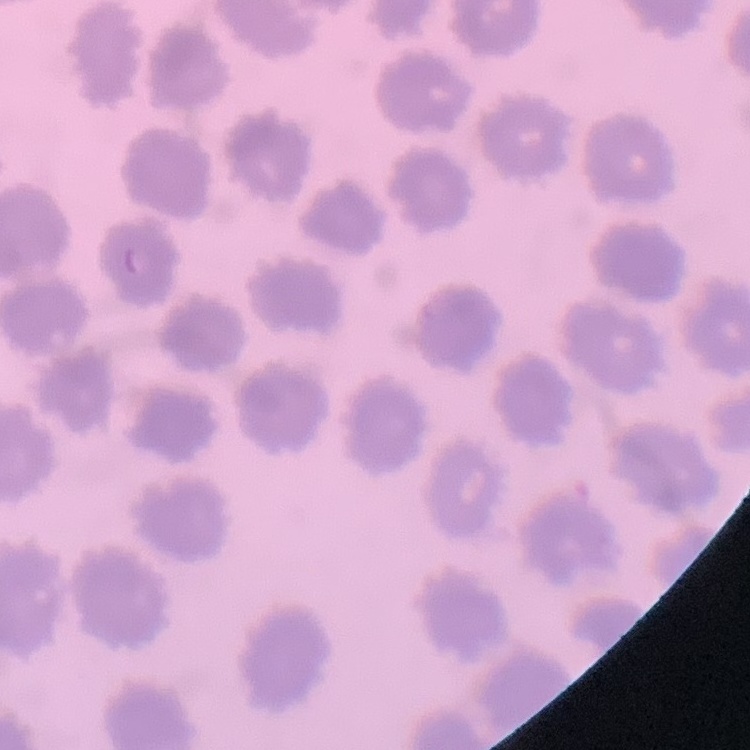 The red blood cells show no rouleaux formation. One tile cut from a larger photomicrograph. Stained with either Field's or Giemsa. Thin blood film.